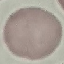

result = no malaria parasites detected
capture = smartphone through the microscope eyepiece
stain = Giemsa
preparation = thin blood smear
image type = automatically extracted cell patch, resized to 64 × 64 pixels